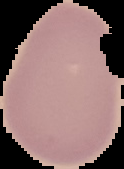

Summary:
  - Image size: 124×169 pixels
  - Result: negative for Plasmodium parasites
  - Preparation: thin blood smear
  - Image type: segmented cell region on a black background